Assess the morphology of the erythrocytes.
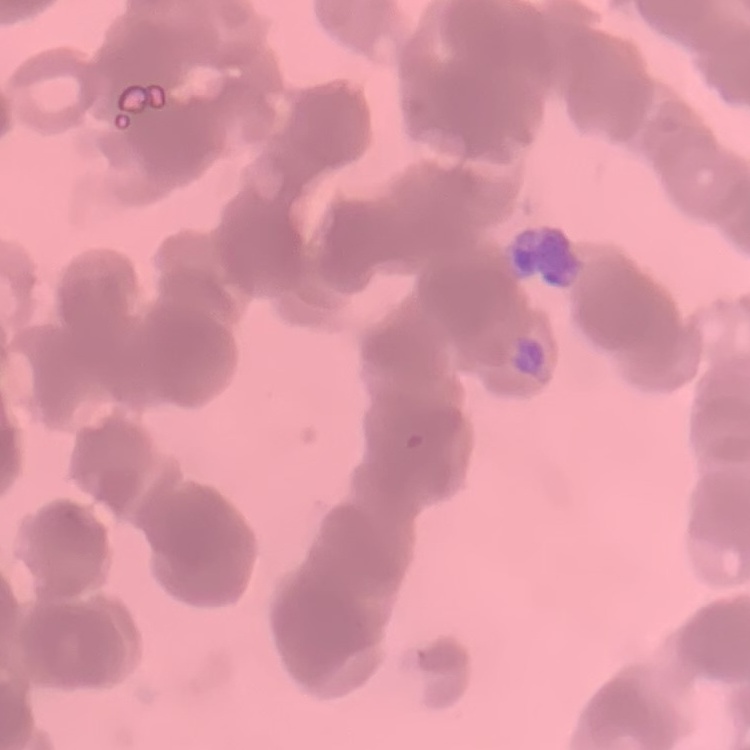
They show rouleaux formation.

Summary:
  - Preparation: thin blood smear
  - Image type: square crop of a larger photomicrograph
  - Stain: Field's or Giemsa